Assess this cell for malaria.
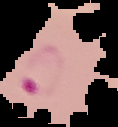

It is parasitized.

Image is 118×127 pixels. Segmented cell region on a black background. From a thin blood smear.